Assess for malaria.
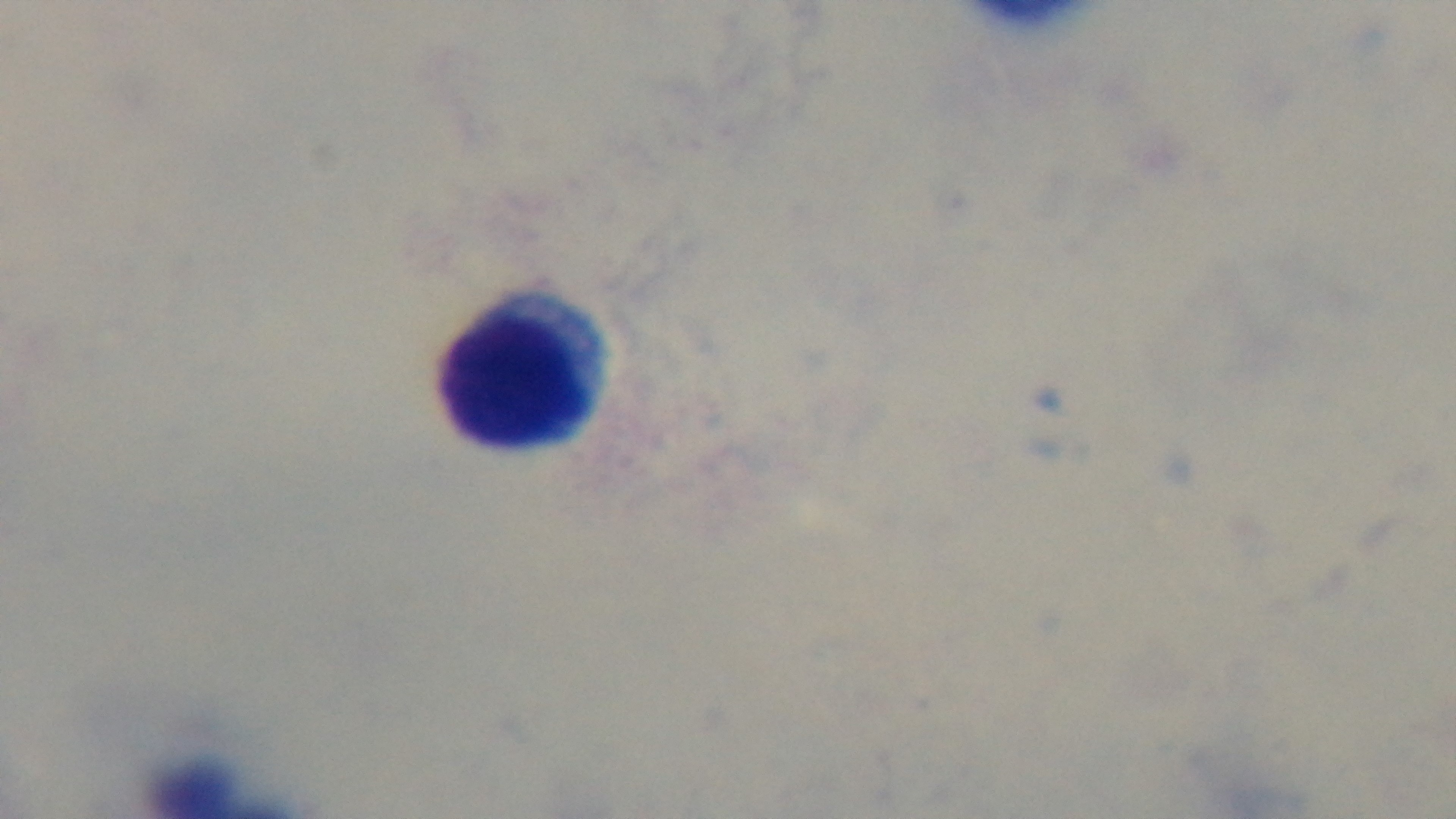

It is uninfected.

capture = mounted 4K digital camera
preparation = thick smear
field of view = single
modality = light microscopy
objective = 100x oil immersion
stain = Giemsa